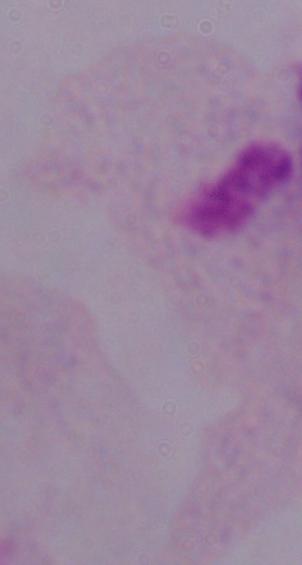
Summary:
  - Magnification: 1000x
  - Identification: trichomonad
  - Modality: photomicrograph